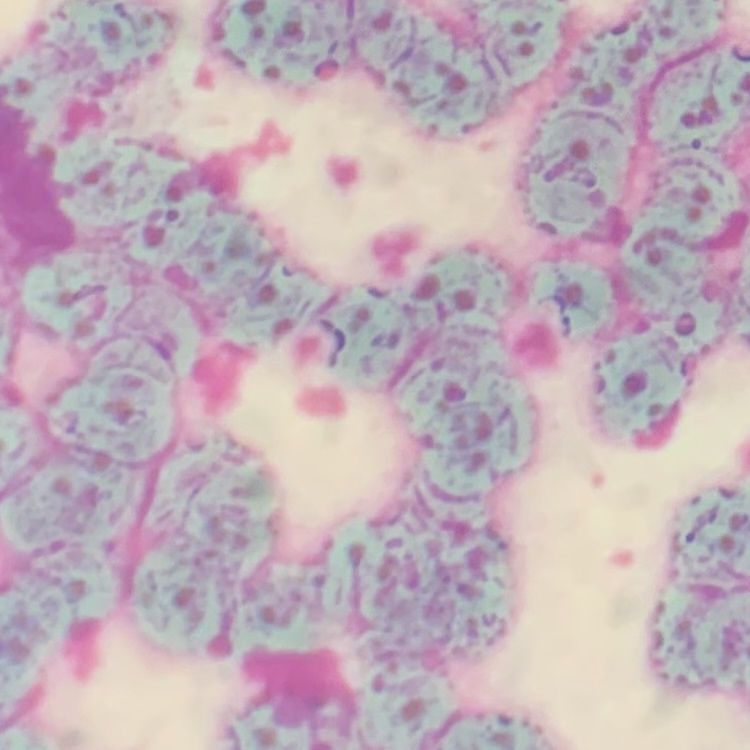

Summary:
  - Erythrocyte morphology: rouleaux formation
  - Image type: square crop of a larger photomicrograph
  - Preparation: thin blood smear
  - Stain: Field's or Giemsa